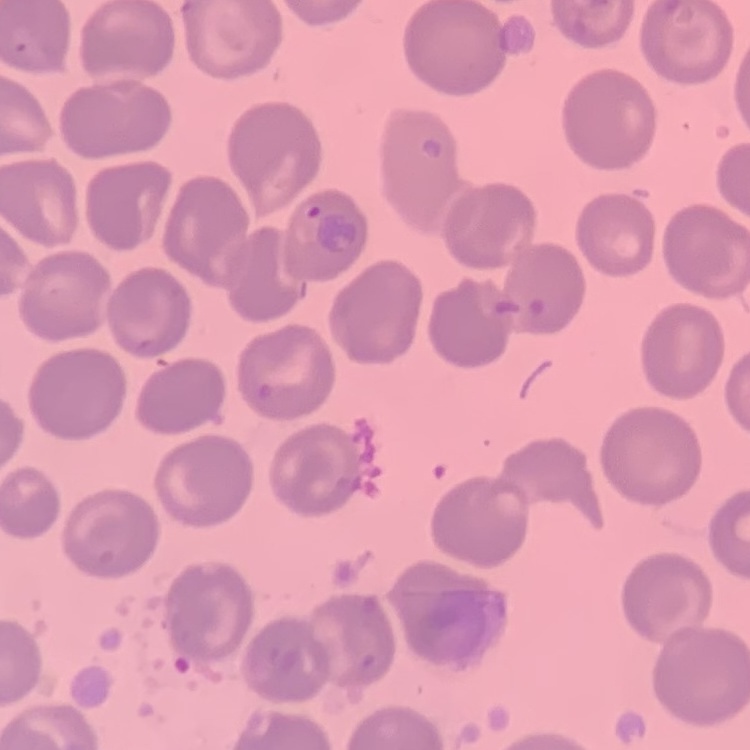

Summary:
  - Erythrocyte morphology: no rouleaux formation
  - Image type: one tile cut from a larger photomicrograph
  - Stain: Field's or Giemsa
  - Preparation: thin blood smear